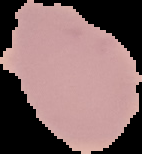 Image is 142×154 pixels. The area outside the segmented cell region is set to black. Result: negative for malaria parasites. From a thin blood film.